Identify the parasite.
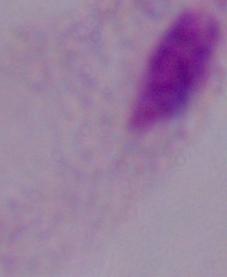

A trichomonad.

modality: micrograph
magnification: 1000x